Classify this cell by malaria status.
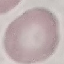

It is uninfected.

Giemsa stain. Cell patch, automatically extracted from a larger field of view and resized to 64 × 64 pixels. Acquired by smartphone through the microscope eyepiece. Thin smear of blood.